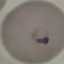
result: malaria parasites identified
stain: Giemsa
image_type: automatically extracted cell patch, resized to 64 × 64 pixels
capture: smartphone camera at the microscope eyepiece
preparation: thin blood film